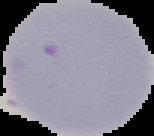
Summary:
  - Preparation: thin blood smear
  - Malaria status: uninfected
  - Image size: 154×136 pixels
  - Image type: segmented cell region with the area outside set to black